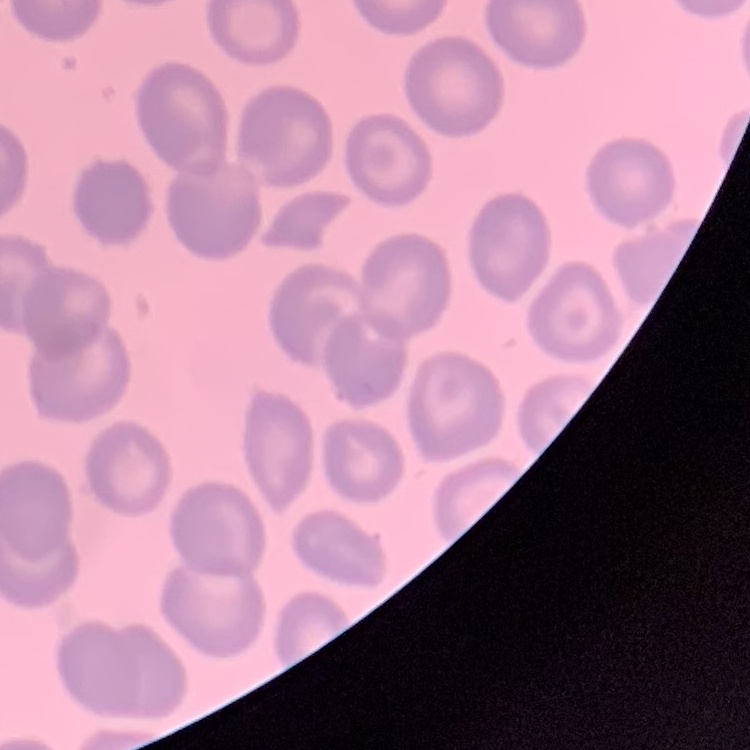

red_blood_cell_morphology: no rouleaux formation
stain: Field's or Giemsa
image_type: square crop of a larger photomicrograph
preparation: thin blood smear